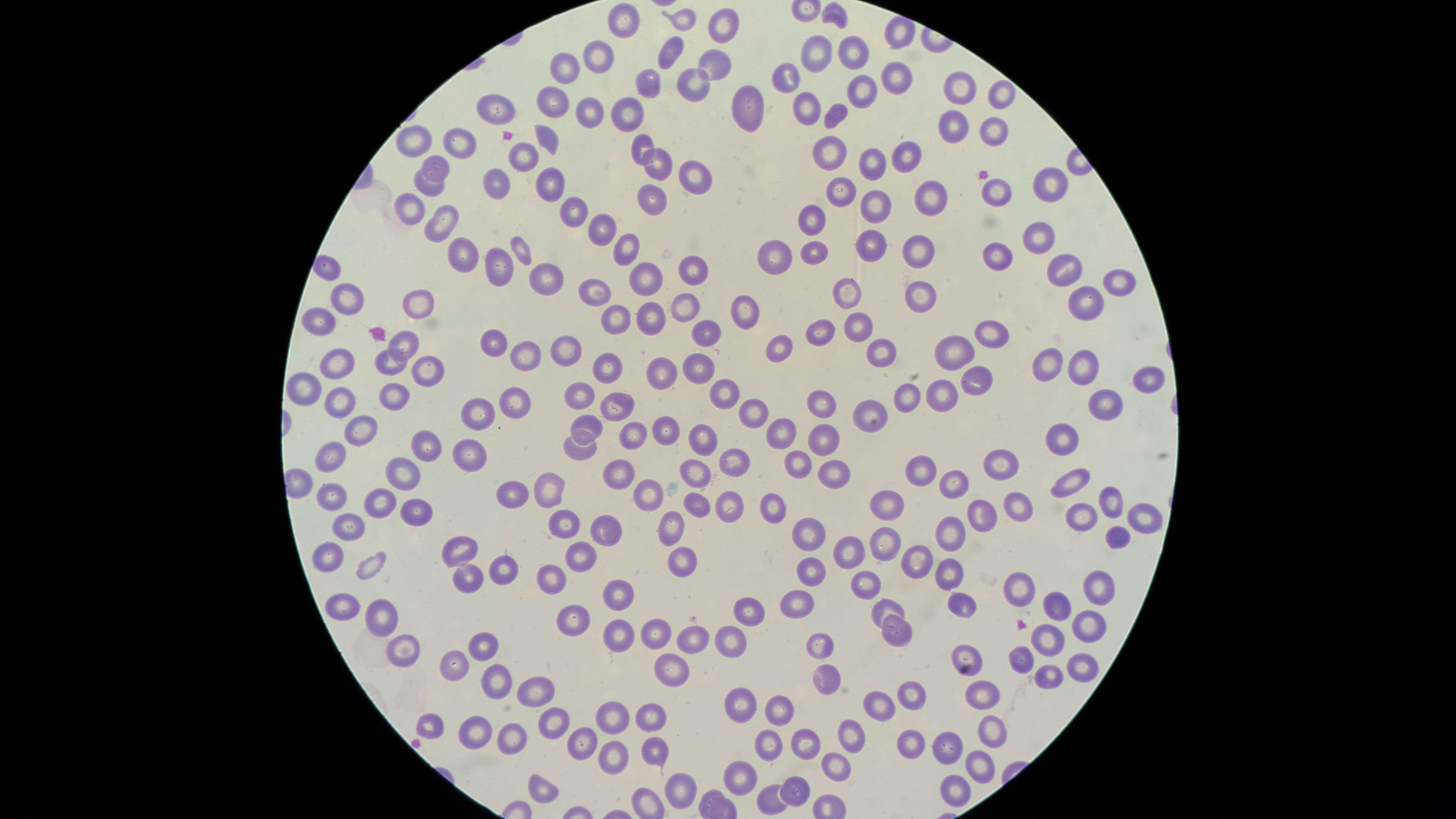
{
  "preparation": "thin smear of blood",
  "stain": "Giemsa",
  "capture": "smartphone photograph through the microscope eyepiece",
  "uninfected_RBCs": "approximate marker points, in pixels from the top-left corner: (x=834, y=11), (x=625, y=20), (x=683, y=21), (x=723, y=27), (x=670, y=47), (x=822, y=51), (x=855, y=53), (x=602, y=57), (x=713, y=64), (x=568, y=67), (x=790, y=76), (x=889, y=76), (x=654, y=82), (x=691, y=84), (x=866, y=85), (x=958, y=90), (x=1000, y=92), (x=555, y=102), (x=809, y=104), (x=494, y=105), (x=749, y=108), (x=631, y=110), (x=591, y=113), (x=834, y=113), (x=953, y=126), (x=993, y=127), (x=547, y=134), (x=420, y=140), (x=465, y=142), (x=642, y=142), (x=833, y=151), (x=903, y=152), (x=523, y=153), (x=874, y=161), (x=659, y=165), (x=434, y=167), (x=696, y=174), (x=548, y=181), (x=1049, y=184), (x=431, y=186), (x=498, y=189), (x=843, y=190), (x=996, y=190), (x=934, y=191), (x=655, y=198), (x=879, y=203), (x=415, y=208), (x=577, y=213), (x=813, y=217), (x=443, y=222), (x=603, y=230), (x=1038, y=235), (x=872, y=244), (x=519, y=248), (x=815, y=248), (x=627, y=250), (x=917, y=250), (x=776, y=253), (x=998, y=253), (x=465, y=256), (x=492, y=264), (x=693, y=270), (x=1066, y=270), (x=646, y=275), (x=551, y=279), (x=1115, y=282), (x=847, y=288), (x=593, y=293), (x=921, y=293), (x=348, y=297), (x=1088, y=302), (x=422, y=304), (x=686, y=305), (x=749, y=308), (x=615, y=316), (x=647, y=317), (x=860, y=325), (x=823, y=326), (x=317, y=327), (x=705, y=331), (x=997, y=337), (x=409, y=338), (x=781, y=342), (x=496, y=343), (x=962, y=349), (x=569, y=351), (x=527, y=353), (x=878, y=354), (x=389, y=361), (x=609, y=363), (x=1051, y=363), (x=336, y=365), (x=697, y=365), (x=1083, y=367), (x=428, y=369), (x=665, y=371), (x=1151, y=377), (x=971, y=378), (x=299, y=385), (x=728, y=390), (x=940, y=392), (x=583, y=393), (x=385, y=394), (x=909, y=395), (x=336, y=399), (x=1105, y=399), (x=513, y=400), (x=823, y=402), (x=615, y=405), (x=869, y=406), (x=749, y=408), (x=477, y=411), (x=362, y=423), (x=589, y=424), (x=666, y=428), (x=777, y=434), (x=822, y=434), (x=1065, y=434), (x=704, y=435), (x=630, y=436), (x=423, y=446), (x=581, y=447), (x=327, y=453), (x=468, y=455), (x=735, y=457), (x=796, y=464), (x=998, y=464), (x=924, y=468), (x=699, y=469), (x=403, y=471), (x=625, y=474), (x=829, y=477), (x=1075, y=480), (x=952, y=482), (x=555, y=488), (x=332, y=493), (x=514, y=494), (x=650, y=495), (x=379, y=501), (x=1112, y=501), (x=699, y=502), (x=732, y=503), (x=886, y=503), (x=1016, y=504), (x=411, y=509), (x=776, y=511), (x=974, y=515), (x=1081, y=515), (x=1145, y=519), (x=566, y=522), (x=346, y=524), (x=671, y=527), (x=606, y=529), (x=809, y=530), (x=949, y=535), (x=1118, y=535), (x=886, y=542), (x=459, y=548), (x=852, y=552), (x=329, y=554), (x=584, y=557), (x=679, y=557), (x=923, y=562), (x=367, y=563), (x=502, y=567), (x=812, y=567), (x=949, y=569), (x=466, y=574), (x=549, y=576), (x=866, y=581), (x=1100, y=583), (x=1025, y=586), (x=621, y=591), (x=799, y=601), (x=1059, y=601), (x=963, y=602), (x=344, y=606), (x=888, y=606), (x=749, y=607), (x=383, y=612), (x=576, y=616), (x=1086, y=624), (x=654, y=631), (x=899, y=632), (x=728, y=634), (x=623, y=635), (x=691, y=635), (x=1049, y=636), (x=819, y=640), (x=404, y=645), (x=482, y=645), (x=968, y=650), (x=1023, y=659), (x=454, y=665), (x=1082, y=665), (x=675, y=667), (x=829, y=670), (x=1048, y=672), (x=488, y=675), (x=531, y=692), (x=982, y=692), (x=911, y=694), (x=878, y=700), (x=744, y=705), (x=782, y=706), (x=650, y=711), (x=616, y=714), (x=548, y=721), (x=427, y=724), (x=469, y=729), (x=995, y=730), (x=852, y=736), (x=586, y=738), (x=513, y=739), (x=768, y=739), (x=951, y=744), (x=915, y=747), (x=806, y=748), (x=655, y=749), (x=611, y=760), (x=982, y=764), (x=838, y=767), (x=741, y=773), (x=797, y=784), (x=679, y=787), (x=957, y=788), (x=538, y=790), (x=769, y=800)",
  "image_size": "1456×819 pixels",
  "visible_region": "circular",
  "field_of_view": "single",
  "presence": "no malaria parasites detected"
}